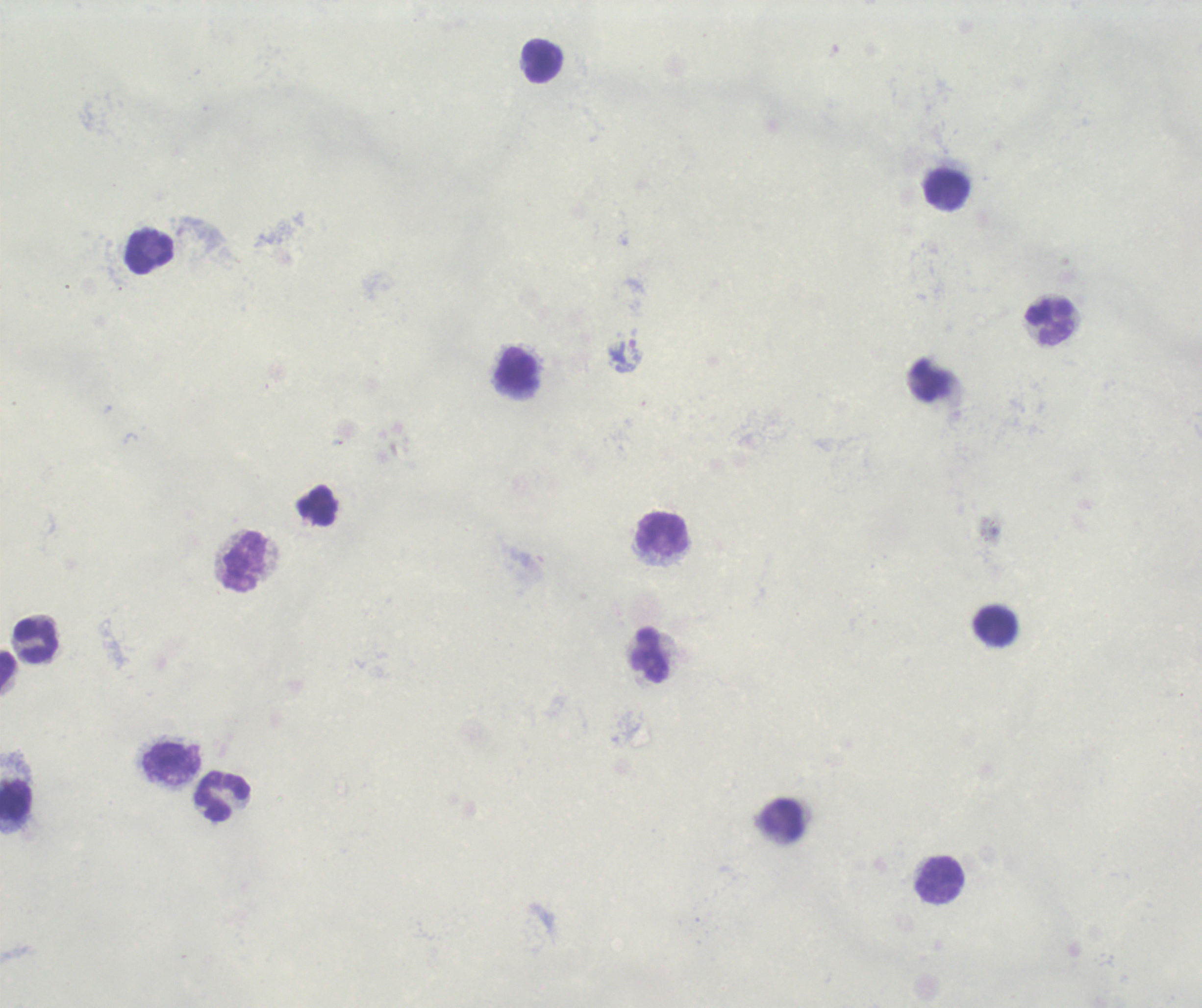

Approximate centers as [x, y] in pixels.
Summary:
  - Leukocyte locations: [543, 62], [947, 190], [150, 251], [1049, 322], [517, 370], [662, 534], [244, 562], [997, 626], [36, 641], [650, 655], [7, 673], [171, 761], [223, 797], [15, 800], [783, 820], [940, 880]
  - Trophozoite locations: [626, 356]
  - Background quality: unsatisfactory
  - Image size: 1202×1008 pixels
  - Magnification: 100x
  - Context: previously used in an actual diagnosis
  - Stain: Romanowsky
  - Result: malaria parasites identified
  - Field of view: single
  - Preparation: thick blood film